Identify the parasite.
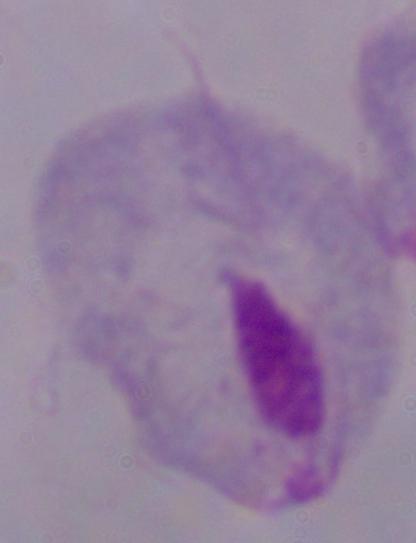

This is a trichomonad.

Summary:
  - Magnification: 1000x
  - Modality: photomicrograph